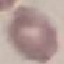
malaria status = uninfected
image type = cell patch, automatically extracted from a larger field of view and resized to 64 × 64 pixels
capture = smartphone through the microscope eyepiece
stain = Giemsa
preparation = thin blood smear